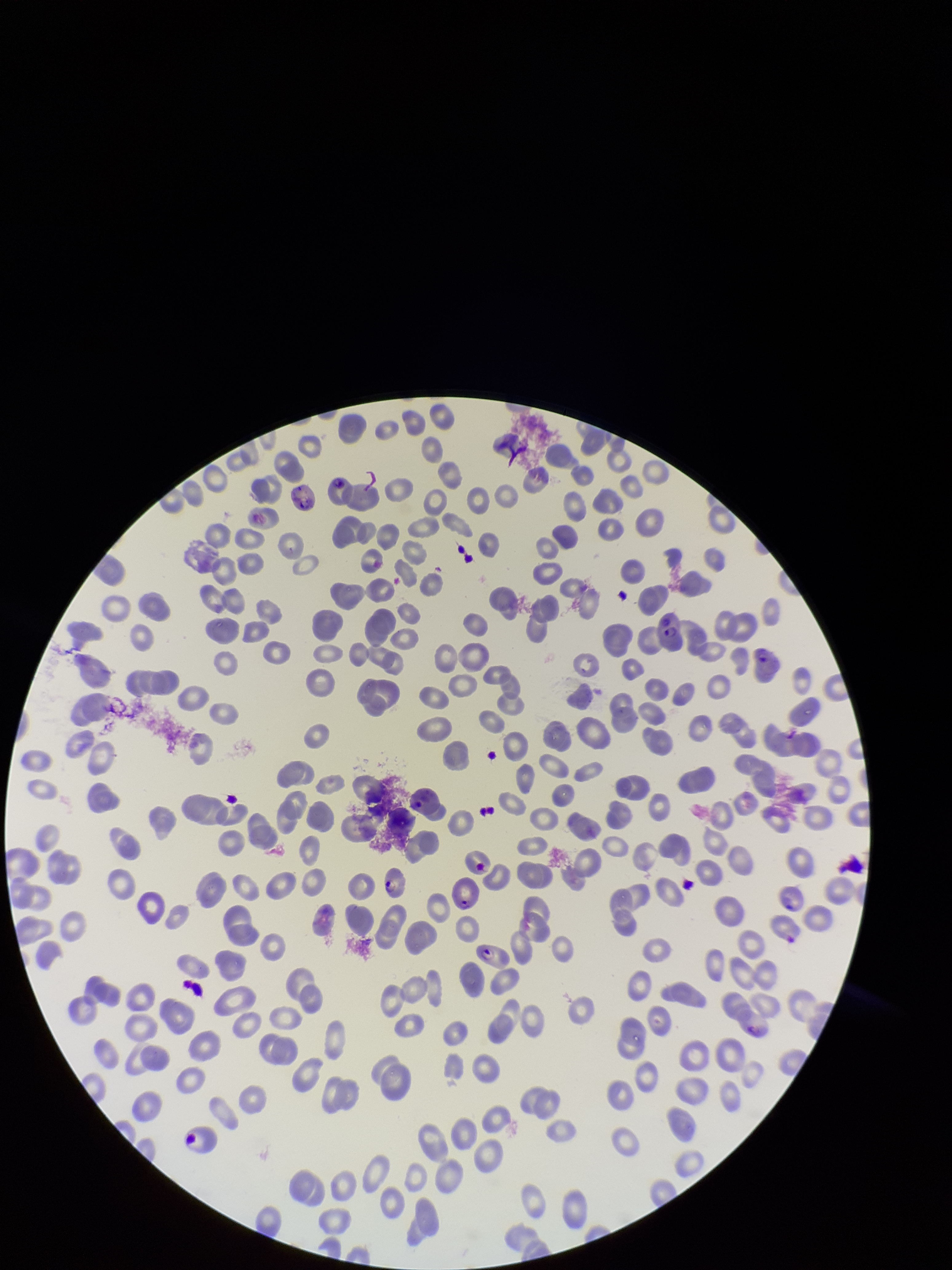
Summary:
  - Field of view: one from this slide
  - Preparation: thin smear
  - Image size: 952×1270 pixels
  - Stain: Giemsa
  - Red blood cell count: 228
  - Capture: smartphone photograph through the microscope eyepiece
  - Patient malaria status: infected
  - Species reported for this patient: Plasmodium falciparum
  - Parasitized red blood cell count: 9
  - Parasitized red blood cells: detected